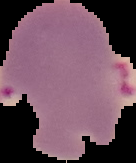
Cell region segmented out of the field of view; the surrounding area is masked to black. From a thin blood smear. Result: Plasmodium parasites identified. Image is 136×163 pixels.